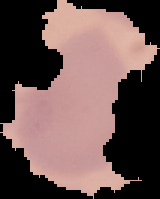

Summary:
  - Malaria status: uninfected
  - Image size: 160×199 pixels
  - Image type: cell region segmented out of the field of view; surrounding area masked to black
  - Preparation: thin blood smear